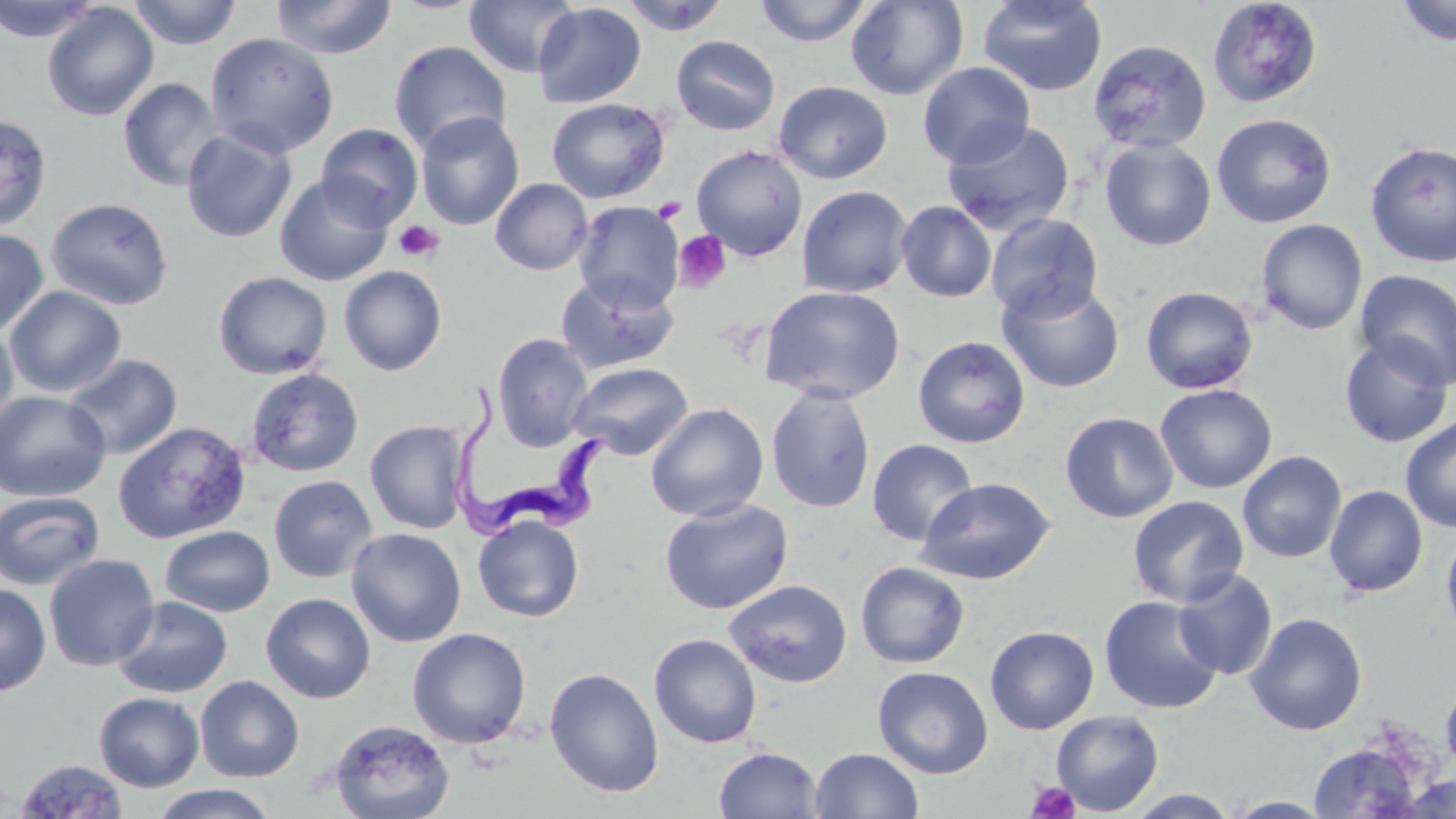 Approximate bounding boxes as (x1, y1, x2, y2) in pixels. Trypanosoma brucei locations: (450, 385, 614, 537). Uninfected red blood cell locations: (0, 0, 102, 43), (128, 0, 243, 49), (270, 0, 396, 60), (463, 0, 580, 78), (620, 0, 730, 35), (755, 0, 872, 46), (846, 0, 968, 100), (977, 0, 1108, 97), (1206, 0, 1323, 109), (1395, 0, 1456, 47), (532, 2, 646, 108), (41, 3, 159, 122), (204, 32, 340, 158), (671, 35, 780, 136), (1088, 39, 1211, 154), (388, 40, 513, 157), (918, 62, 1035, 168), (118, 77, 224, 192), (773, 80, 893, 184), (546, 98, 670, 203), (416, 111, 524, 230), (1212, 113, 1337, 229), (0, 114, 53, 232), (941, 119, 1075, 235), (315, 123, 423, 229), (181, 128, 297, 243), (1100, 139, 1216, 251), (1364, 141, 1456, 268), (691, 145, 808, 260), (274, 175, 393, 287), (490, 178, 593, 275), (797, 185, 913, 298), (45, 197, 174, 310), (573, 200, 685, 312), (896, 201, 996, 302), (985, 213, 1103, 323), (1256, 218, 1368, 335), (0, 228, 50, 336), (338, 265, 447, 376), (1354, 268, 1456, 390), (213, 270, 332, 379), (555, 271, 679, 374), (997, 280, 1125, 393), (758, 284, 906, 404), (1140, 285, 1258, 395), (4, 286, 127, 397), (0, 322, 19, 437), (492, 332, 594, 451), (1338, 334, 1454, 448), (913, 335, 1031, 448), (63, 353, 183, 459), (567, 361, 692, 460), (246, 367, 364, 477), (1155, 384, 1277, 494), (766, 385, 876, 513), (0, 390, 111, 502), (646, 402, 768, 521), (1060, 411, 1178, 523), (1400, 414, 1456, 533), (365, 419, 472, 534), (112, 420, 251, 543), (867, 439, 978, 546), (1237, 451, 1347, 563), (268, 475, 377, 583), (915, 476, 1056, 585), (1324, 485, 1429, 597), (0, 491, 106, 590), (1127, 495, 1248, 607), (659, 498, 794, 614), (473, 515, 584, 622), (1440, 523, 1456, 647), (159, 525, 275, 617), (346, 528, 466, 647), (43, 552, 160, 672), (855, 561, 970, 669), (1172, 569, 1278, 680), (724, 578, 853, 688), (0, 583, 51, 696), (261, 592, 375, 704), (112, 595, 233, 698), (1099, 595, 1224, 714), (1244, 612, 1367, 735), (984, 625, 1099, 734), (407, 627, 531, 748), (649, 633, 762, 748), (872, 665, 993, 779), (544, 666, 664, 798), (194, 675, 304, 782), (1441, 680, 1456, 776), (93, 692, 204, 792), (1051, 709, 1164, 816), (330, 719, 455, 819), (1308, 742, 1423, 818), (713, 746, 822, 819), (810, 747, 924, 819), (14, 758, 129, 818), (1397, 773, 1456, 818), (147, 784, 280, 819), (1122, 788, 1241, 818), (1223, 795, 1337, 818). Platelet locations: (652, 197, 687, 224), (393, 220, 444, 263), (673, 230, 730, 294), (1026, 781, 1081, 819). Slide-level diagnosis: Trypanosoma brucei. Image is 1456×819 pixels. Thin blood film. Single field of view. May-Grünwald-Giemsa-stained preparation. Optical microscopy. Captured at 1000x magnification.